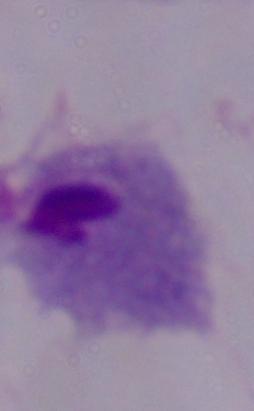 Captured at 1000x magnification. Micrograph. A trichomonad is shown.